Classify this cell by malaria status.
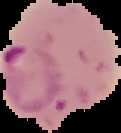

Parasitized.

Image is 121×133 pixels. From a thin blood film. The area outside the segmented cell region is set to black.